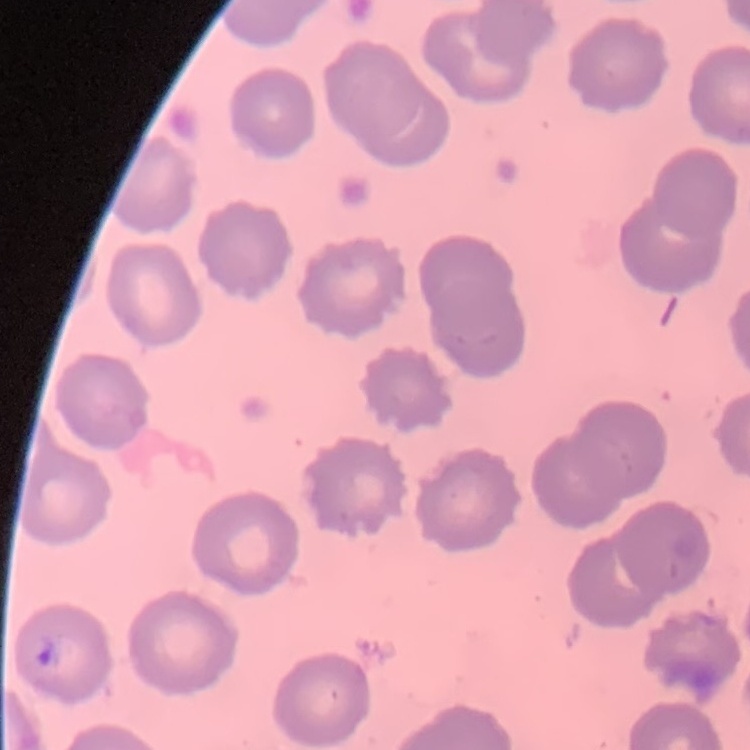
{
  "red_blood_cell_morphology": "no rouleaux formation",
  "image_type": "one tile cut from a larger photomicrograph",
  "preparation": "thin blood smear",
  "stain": "Field's or Giemsa"
}